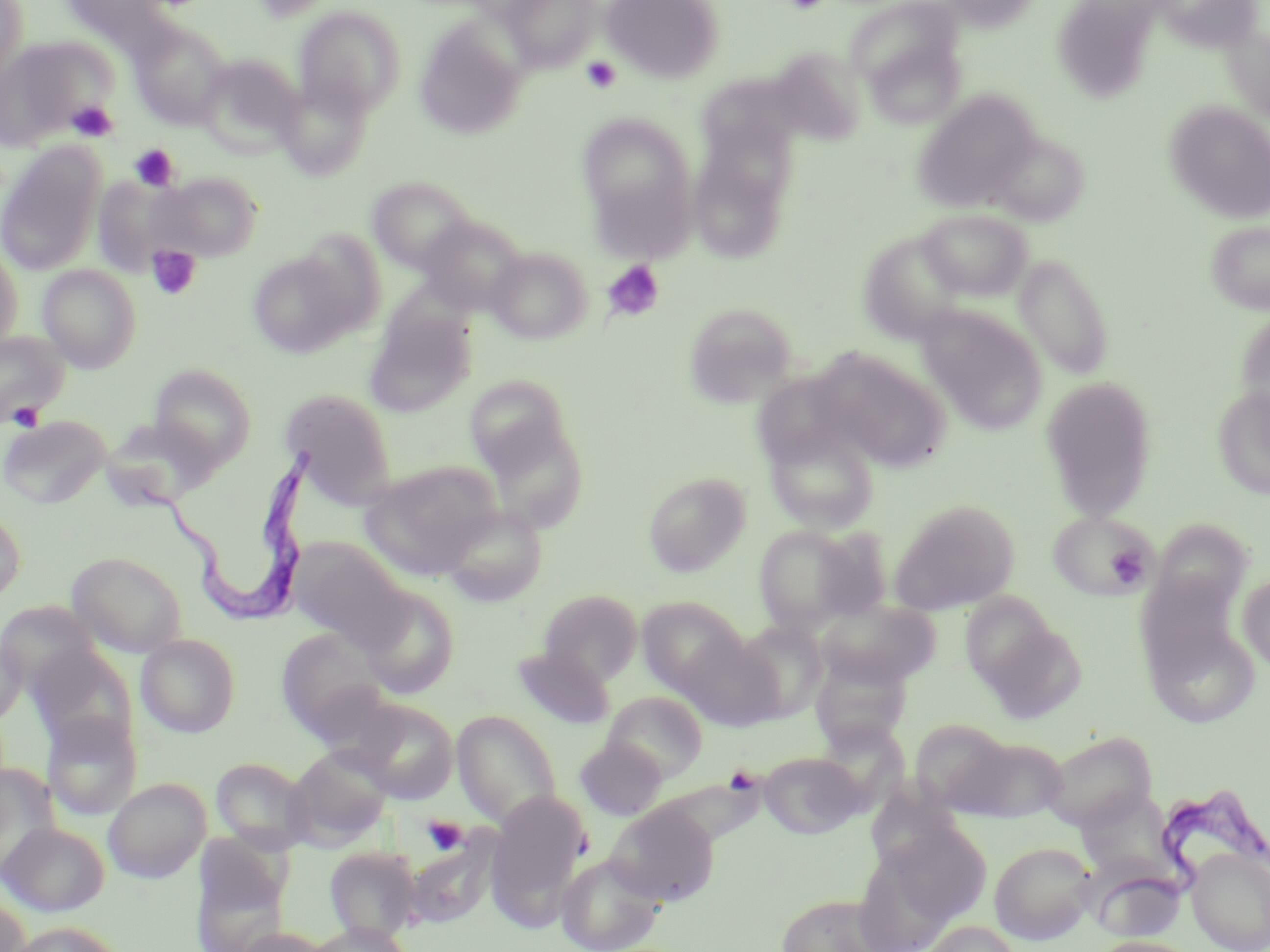
Summary:
  - Coordinate format: approximate bounding boxes as [x1, y1, x2, y2] in pixels
  - Trypanosoma brucei locations: [125, 444, 317, 625], [1090, 792, 1270, 926]
  - Uninfected red blood cell locations: [0, 0, 28, 91], [58, 0, 176, 46], [248, 0, 343, 23], [601, 0, 724, 83], [931, 0, 1045, 32], [1160, 0, 1263, 52], [502, 1, 601, 70], [1062, 3, 1162, 97], [293, 5, 405, 116], [414, 17, 528, 140], [857, 17, 967, 128], [131, 22, 231, 129], [1223, 24, 1269, 125], [0, 37, 113, 148], [768, 47, 866, 145], [196, 56, 301, 158], [695, 75, 803, 179], [275, 78, 374, 180], [912, 91, 1040, 213], [1164, 101, 1270, 224], [578, 113, 697, 249], [688, 126, 795, 264], [994, 135, 1088, 224], [0, 142, 105, 277], [154, 171, 262, 261], [92, 174, 190, 277], [367, 176, 476, 274], [918, 208, 1032, 301], [417, 216, 526, 315], [1205, 220, 1270, 315], [294, 230, 387, 334], [858, 230, 972, 344], [0, 241, 24, 353], [486, 246, 592, 344], [247, 250, 366, 358], [1014, 253, 1114, 379], [37, 265, 142, 372], [683, 302, 797, 408], [916, 305, 1047, 433], [365, 307, 476, 418], [1235, 309, 1270, 419], [0, 330, 70, 427], [812, 350, 952, 474], [150, 364, 256, 468], [750, 370, 861, 471], [465, 376, 574, 479], [1040, 376, 1158, 522], [1211, 384, 1270, 499], [280, 388, 397, 504], [475, 407, 590, 532], [0, 415, 110, 508], [99, 416, 221, 508], [766, 427, 879, 533], [359, 461, 500, 578], [643, 471, 751, 577], [890, 500, 1019, 614], [0, 504, 26, 604], [441, 504, 547, 606], [1049, 512, 1158, 600], [751, 524, 873, 634], [806, 525, 894, 622], [288, 537, 409, 648], [67, 551, 187, 657], [1134, 568, 1246, 688], [1237, 572, 1270, 672], [358, 584, 460, 698], [539, 589, 643, 685], [959, 591, 1061, 693], [636, 596, 748, 696], [814, 598, 941, 689], [1142, 610, 1259, 729], [973, 614, 1087, 724], [734, 619, 828, 721], [277, 627, 389, 741], [0, 632, 27, 725], [678, 632, 784, 730], [136, 633, 241, 737], [25, 644, 136, 754], [512, 646, 615, 729], [809, 653, 911, 751], [603, 691, 708, 782], [350, 699, 459, 804], [453, 710, 562, 828], [42, 711, 142, 821], [910, 718, 1014, 814], [1041, 729, 1158, 830], [957, 736, 1069, 822], [575, 737, 665, 818], [285, 745, 394, 847], [759, 751, 866, 838], [211, 757, 313, 854], [0, 764, 60, 875], [103, 778, 210, 882], [487, 792, 589, 921], [606, 803, 719, 906], [1, 822, 109, 916], [852, 839, 964, 952], [990, 841, 1097, 944], [191, 845, 292, 952], [325, 847, 423, 943], [410, 847, 490, 925], [1187, 849, 1270, 952], [556, 854, 663, 952], [1090, 867, 1187, 941], [776, 893, 894, 952], [0, 894, 30, 952], [922, 919, 1022, 952], [10, 921, 124, 952], [308, 923, 413, 952], [234, 927, 333, 952], [1091, 936, 1203, 952]
  - Platelet locations: [783, 0, 831, 14], [581, 57, 622, 94], [67, 100, 118, 141], [129, 144, 179, 191], [147, 245, 202, 300], [602, 260, 665, 322], [7, 403, 44, 432], [1107, 546, 1147, 586], [422, 815, 469, 855]
  - Slide-level diagnosis: Trypanosoma brucei
  - Stain: May-Grünwald-Giemsa
  - Field of view: single
  - Image size: 1270×952 pixels
  - Preparation: thin blood film
  - Modality: optical microscopy
  - Magnification: 1000x